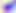 Micrograph. Toxoplasma gondii is shown. Captured at 400x magnification.